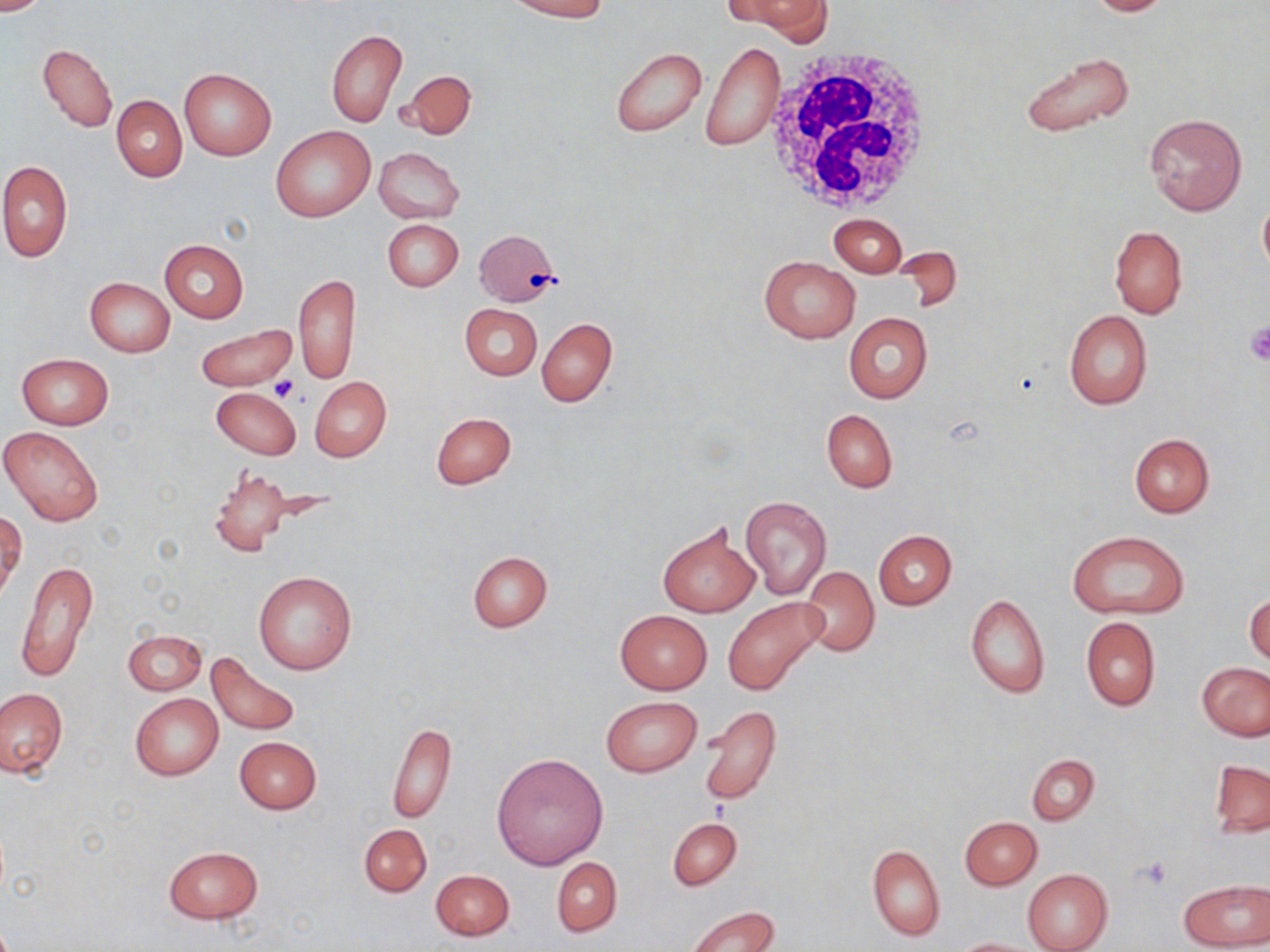

slide-level diagnosis = negative for blood parasites
white blood cell locations = approximate bounding boxes as named x1/y1/x2/y2 corners in pixels: (x1=765, y1=45, x2=937, y2=217)
uninfected red blood cell locations = approximate bounding boxes as named x1/y1/x2/y2 corners in pixels: (x1=0, y1=0, x2=56, y2=14), (x1=509, y1=0, x2=610, y2=20), (x1=733, y1=0, x2=831, y2=39), (x1=1084, y1=0, x2=1179, y2=16), (x1=326, y1=29, x2=407, y2=128), (x1=702, y1=40, x2=784, y2=151), (x1=38, y1=44, x2=118, y2=133), (x1=611, y1=48, x2=707, y2=138), (x1=1020, y1=50, x2=1138, y2=139), (x1=178, y1=68, x2=276, y2=161), (x1=399, y1=69, x2=477, y2=140), (x1=112, y1=95, x2=187, y2=182), (x1=1144, y1=111, x2=1248, y2=216), (x1=270, y1=126, x2=376, y2=222), (x1=373, y1=147, x2=465, y2=224), (x1=0, y1=160, x2=72, y2=264), (x1=1257, y1=197, x2=1270, y2=279), (x1=829, y1=213, x2=906, y2=276), (x1=382, y1=218, x2=464, y2=292), (x1=1109, y1=226, x2=1187, y2=319), (x1=474, y1=229, x2=559, y2=306), (x1=160, y1=240, x2=249, y2=322), (x1=759, y1=255, x2=860, y2=343), (x1=294, y1=273, x2=359, y2=385), (x1=85, y1=277, x2=174, y2=356), (x1=460, y1=303, x2=542, y2=380), (x1=1064, y1=309, x2=1153, y2=410), (x1=843, y1=312, x2=932, y2=404), (x1=537, y1=318, x2=617, y2=407), (x1=194, y1=325, x2=299, y2=391), (x1=18, y1=354, x2=113, y2=430), (x1=310, y1=375, x2=391, y2=462), (x1=212, y1=388, x2=299, y2=459), (x1=821, y1=409, x2=897, y2=493), (x1=431, y1=411, x2=517, y2=489), (x1=1, y1=425, x2=105, y2=526), (x1=1128, y1=433, x2=1215, y2=518), (x1=207, y1=466, x2=295, y2=557), (x1=740, y1=494, x2=832, y2=599), (x1=0, y1=511, x2=25, y2=600), (x1=657, y1=522, x2=760, y2=618), (x1=873, y1=529, x2=956, y2=610), (x1=1069, y1=530, x2=1188, y2=619), (x1=467, y1=551, x2=552, y2=632), (x1=15, y1=559, x2=100, y2=683), (x1=800, y1=566, x2=878, y2=655), (x1=253, y1=571, x2=358, y2=675), (x1=965, y1=592, x2=1050, y2=699), (x1=1246, y1=592, x2=1269, y2=666), (x1=723, y1=597, x2=825, y2=695), (x1=615, y1=610, x2=711, y2=694), (x1=1081, y1=617, x2=1160, y2=710), (x1=123, y1=630, x2=206, y2=695), (x1=206, y1=653, x2=301, y2=736), (x1=1198, y1=663, x2=1269, y2=740), (x1=0, y1=686, x2=66, y2=779), (x1=129, y1=692, x2=224, y2=780), (x1=601, y1=696, x2=702, y2=776), (x1=698, y1=706, x2=781, y2=806), (x1=386, y1=722, x2=456, y2=823), (x1=234, y1=736, x2=321, y2=814), (x1=492, y1=754, x2=607, y2=869), (x1=1027, y1=754, x2=1099, y2=824), (x1=1209, y1=759, x2=1269, y2=837), (x1=668, y1=817, x2=741, y2=889), (x1=961, y1=817, x2=1041, y2=889), (x1=357, y1=823, x2=431, y2=898), (x1=867, y1=844, x2=945, y2=940), (x1=163, y1=846, x2=264, y2=924), (x1=553, y1=857, x2=622, y2=936), (x1=1022, y1=868, x2=1112, y2=952), (x1=431, y1=869, x2=514, y2=941), (x1=1181, y1=881, x2=1269, y2=950), (x1=686, y1=906, x2=780, y2=952), (x1=951, y1=937, x2=1041, y2=951)
preparation = thin blood film
modality = light microscopy
stain = May-Grünwald-Giemsa
image size = 1270×952 pixels
magnification = 1000x
field of view = single
platelet locations = approximate bounding boxes as named x1/y1/x2/y2 corners in pixels: (x1=1245, y1=322, x2=1270, y2=364), (x1=270, y1=377, x2=298, y2=401), (x1=1137, y1=857, x2=1172, y2=892)